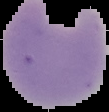
Result: no malaria parasites seen. Image is 109×112 pixels. From a thin blood film. Cell region segmented out of the field of view; the surrounding area is masked to black.